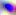

identification: Toxoplasma gondii
modality: photomicrograph
magnification: 400x